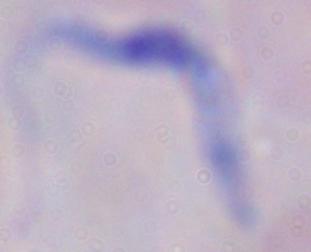

magnification: 1000x
identification: trypanosome
modality: photomicrograph